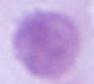
{
  "identification": "erythrocyte",
  "modality": "micrograph",
  "magnification": "1000x"
}